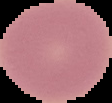

From a thin blood smear. Cell region segmented out of the field of view; the surrounding area is masked to black. Image is 112×103 pixels. Result: negative for Plasmodium parasites.